State which parasite is depicted.
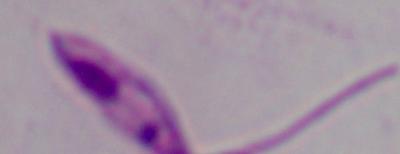

This is Leishmania.

Photomicrograph. Captured at 1000x magnification.